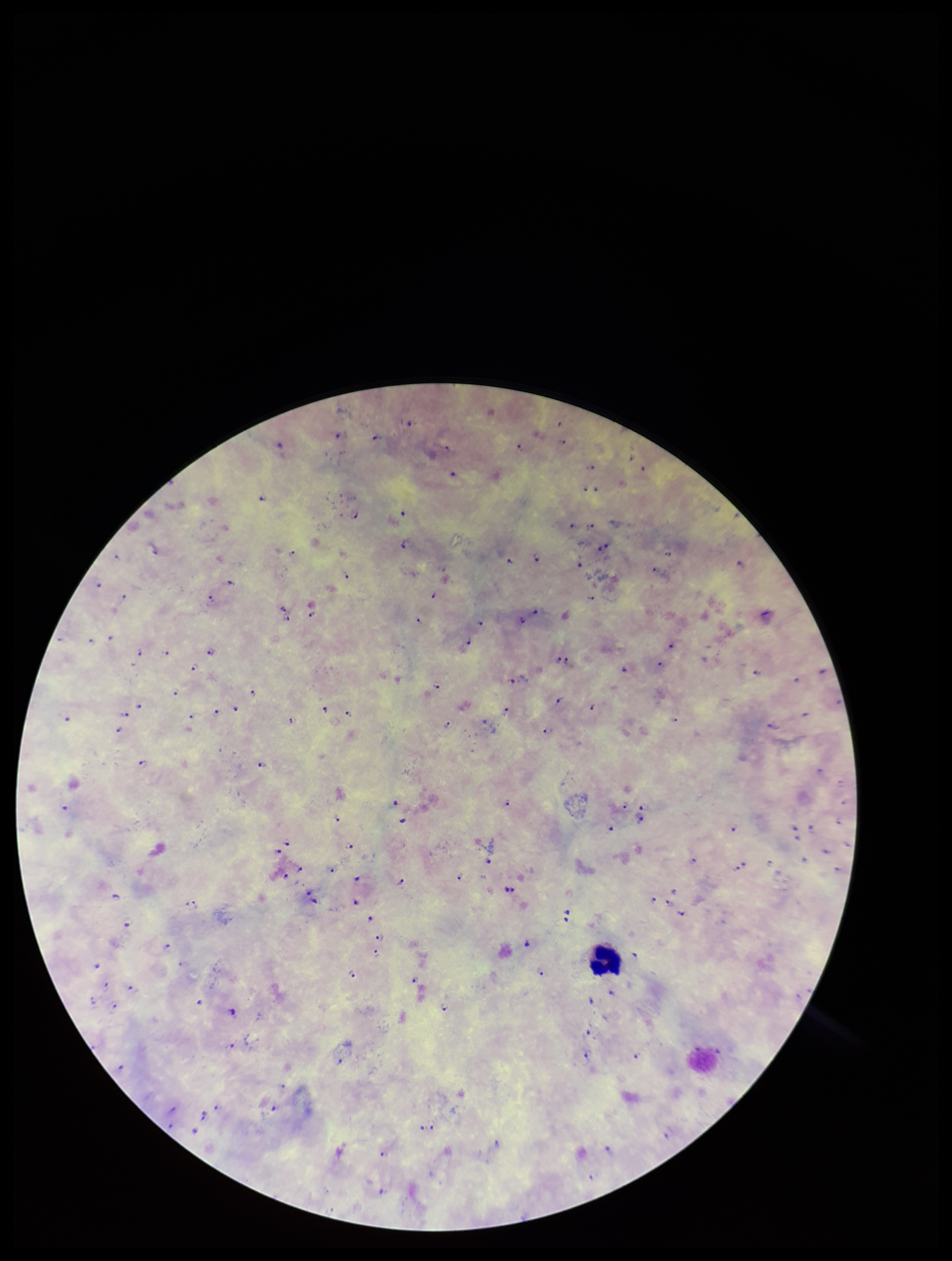
Image is 952×1261 pixels. Giemsa stain. One field from this slide. Preparation: thick smear. Leukocyte count: 1. Species reported for this patient: Plasmodium falciparum. Parasite count: 102. Plasmodium parasites: identified. Patient malaria status: infected. Smartphone photograph taken through the eyepiece of a microscope.